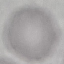

{
  "malaria_status": "uninfected",
  "image_type": "cell patch, automatically extracted from a larger field of view and resized to 64 × 64 pixels",
  "preparation": "thin blood film",
  "stain": "Giemsa",
  "capture": "smartphone camera at the microscope eyepiece"
}